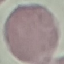

result = negative for malaria parasites
image type = cell patch, automatically extracted from a larger field of view and resized to 64 × 64 pixels
capture = smartphone camera at the microscope eyepiece
stain = Giemsa
preparation = thin smear